Assess the morphology of the erythrocytes.
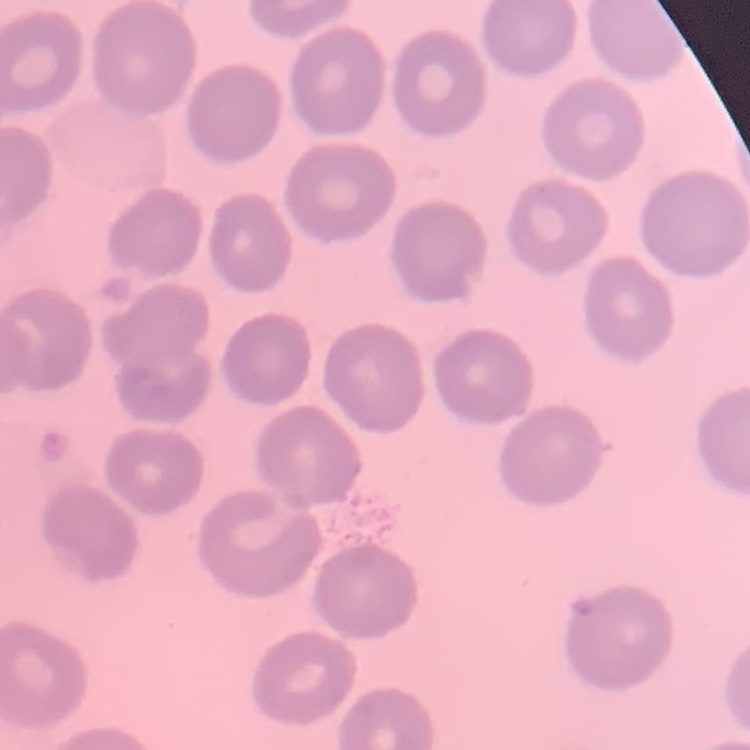
No rouleaux formation.

Field's or Giemsa stain. Square crop of a larger photomicrograph. Thin blood film.